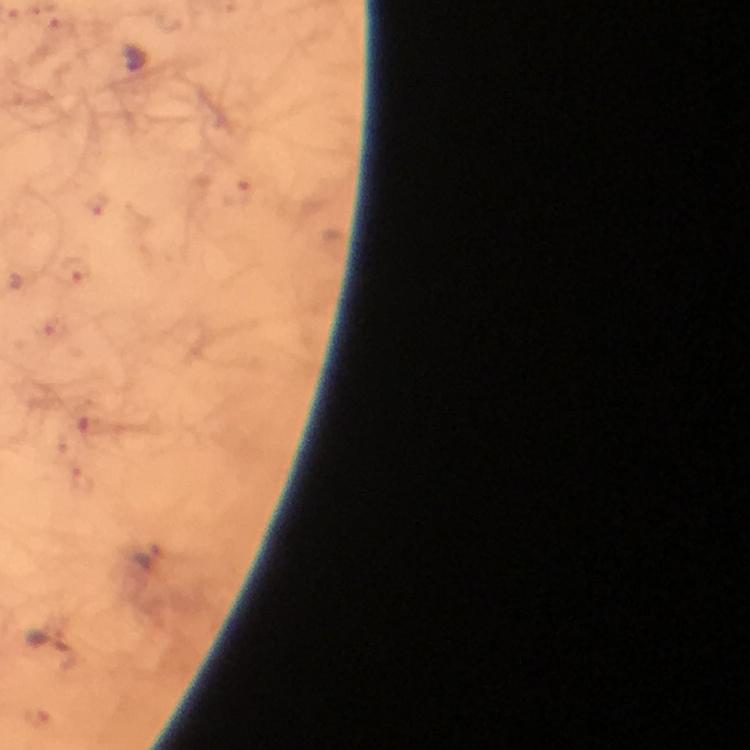 Approximate centers as [x, y] in pixels. Malaria parasite locations: [238, 195], [96, 205], [72, 271], [54, 331], [88, 427], [81, 481], [147, 555], [35, 718]. Giemsa-stained preparation. From a diagnostic examination for malaria. Thick smear. Image is 750×750 pixels. At 100x magnification. Photographed through the microscope with a smartphone camera. Immersion oil was used. Cropped region of a single field of view.